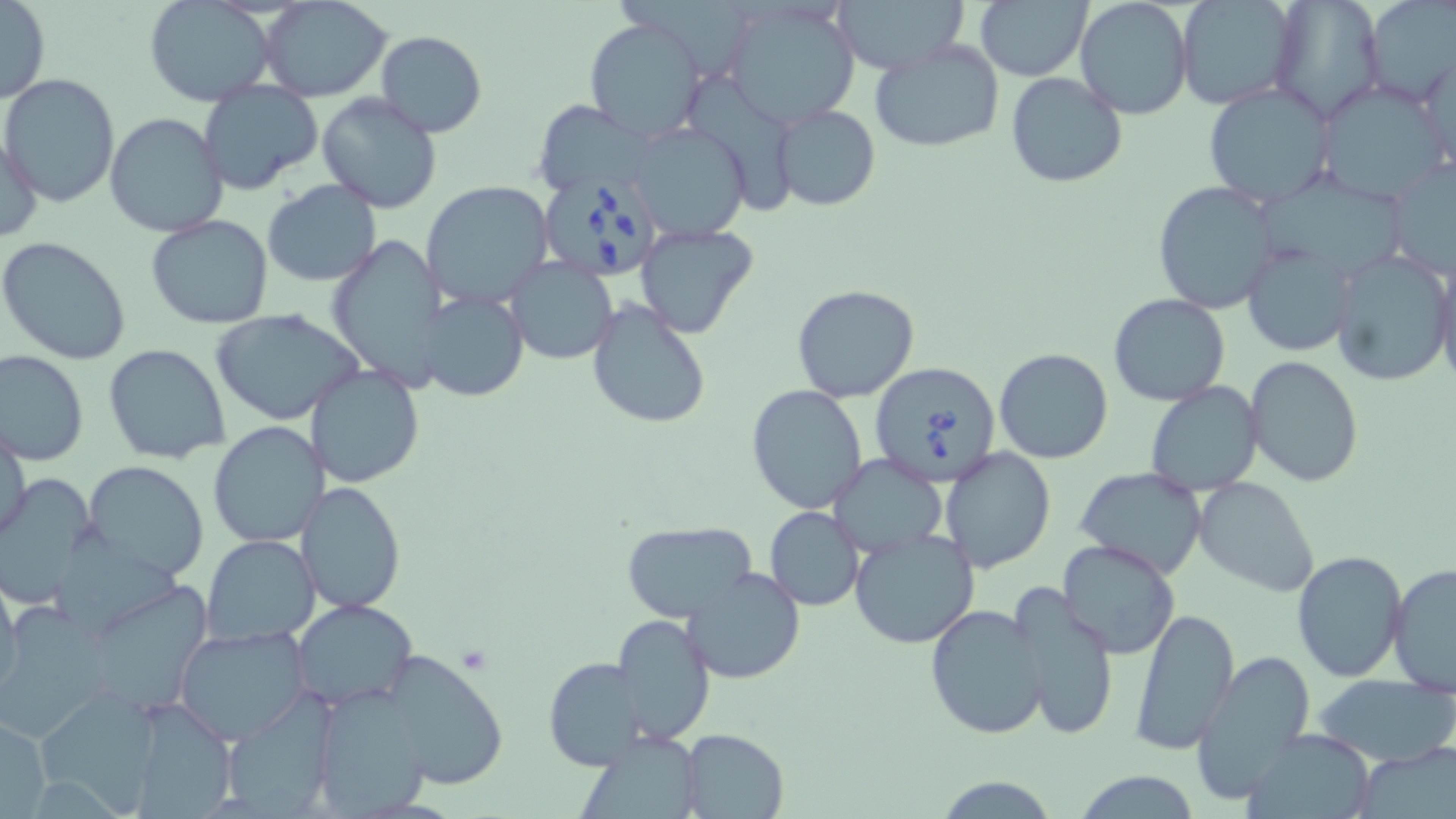

Approximate bounding boxes as (x1,y1)-(x2,y2) corner pairs in pixels. Uninfected red blood cell locations: (721,0)-(862,128), (831,0)-(967,76), (1361,0)-(1453,110), (0,1)-(50,105), (258,1)-(394,102), (975,1)-(1090,80), (1075,1)-(1194,120), (1177,1)-(1303,111), (1267,1)-(1383,123), (144,2)-(275,107), (584,18)-(707,142), (374,31)-(488,137), (869,39)-(1005,155), (1419,48)-(1456,175), (1005,70)-(1129,189), (1,73)-(120,208), (686,74)-(803,226), (1315,78)-(1452,204), (197,80)-(323,196), (1203,81)-(1335,207), (316,91)-(443,213), (534,100)-(655,198), (770,105)-(879,211), (104,112)-(229,238), (627,122)-(751,241), (1,134)-(44,245), (1385,157)-(1455,276), (1258,168)-(1411,276), (421,179)-(554,307), (262,181)-(382,287), (1153,181)-(1280,312), (146,214)-(274,329), (633,222)-(760,339), (325,234)-(448,390), (0,236)-(132,365), (1242,242)-(1352,357), (1329,248)-(1454,388), (1434,254)-(1456,392), (504,257)-(618,364), (793,283)-(922,403), (418,290)-(529,402), (1108,293)-(1232,407), (586,299)-(712,431), (210,309)-(365,426), (104,343)-(233,465), (992,348)-(1114,464), (1,349)-(88,465), (1244,356)-(1364,486), (308,363)-(425,488), (1144,382)-(1264,497), (747,385)-(868,515), (208,422)-(327,548), (1,424)-(29,547), (939,446)-(1055,572), (828,454)-(947,557), (86,461)-(211,583), (1075,467)-(1208,581), (0,474)-(103,606), (1192,476)-(1319,596), (298,482)-(407,613), (765,507)-(865,611), (620,520)-(758,624), (849,527)-(980,647), (59,530)-(196,630), (201,534)-(322,645), (1058,539)-(1181,659), (1292,550)-(1408,683), (1387,563)-(1456,698), (684,567)-(805,684), (0,575)-(21,700), (1009,583)-(1118,740), (100,588)-(214,725), (291,598)-(417,710), (0,600)-(124,745), (925,603)-(1049,739), (1129,607)-(1240,756), (614,613)-(714,744), (172,625)-(312,745), (379,648)-(508,791), (1194,650)-(1316,805), (544,657)-(645,770), (1313,674)-(1456,769), (309,679)-(441,819), (35,690)-(163,814), (121,698)-(241,817), (218,698)-(335,815), (0,715)-(51,814), (577,728)-(704,818), (680,728)-(789,819), (1239,728)-(1377,819), (1351,745)-(1456,819), (1072,770)-(1203,818), (933,775)-(1058,817). Babesia divergens-infected red blood cell locations: (540,177)-(663,282), (870,362)-(1001,487). Slide-level diagnosis: Babesia divergens. May-Grünwald-Giemsa-stained preparation. Image is 1456×819 pixels. Optical microscopy. Captured at 1000x magnification. Single field of view. Thin blood film.